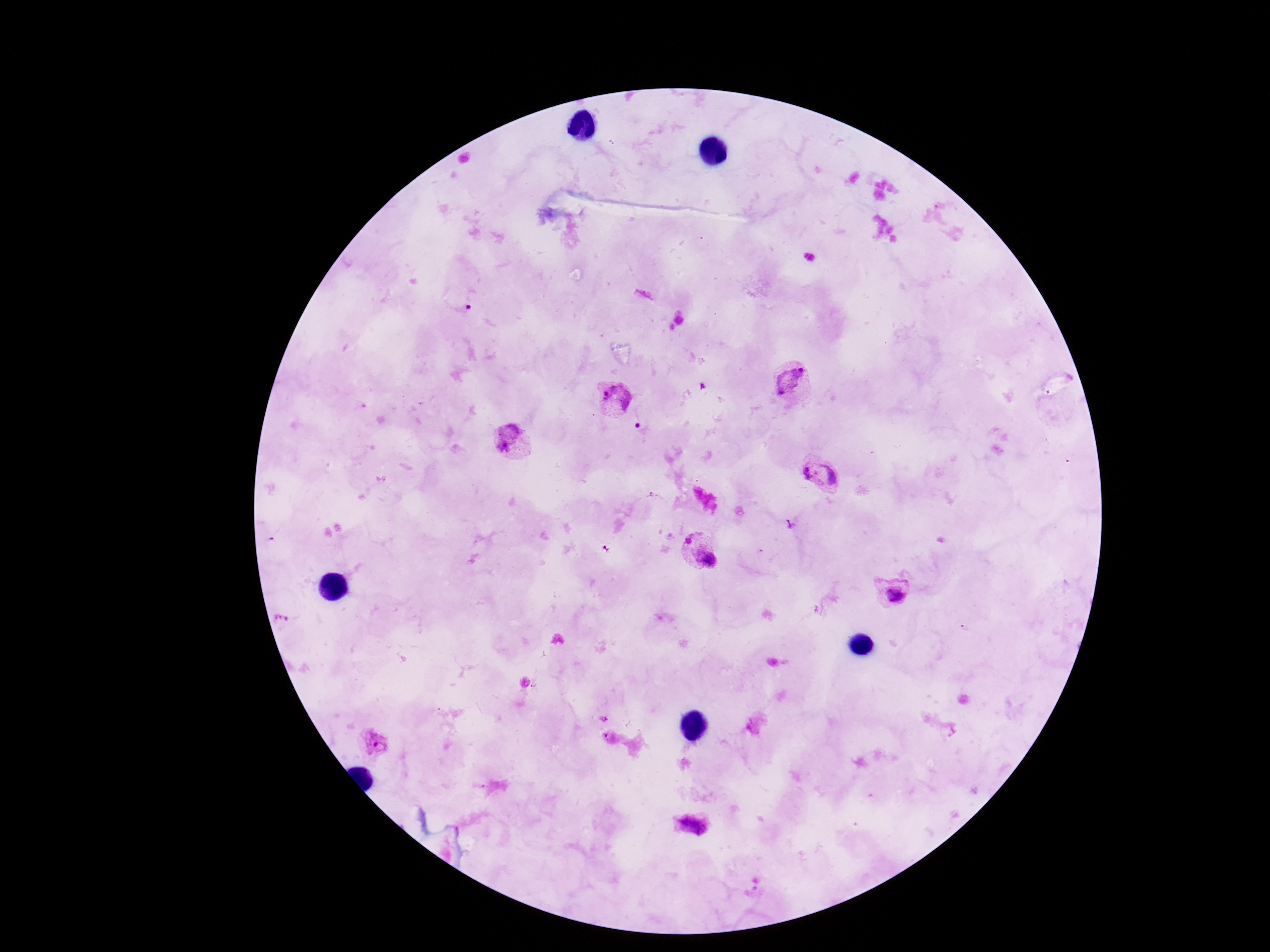
Approximate centers as (x, y) in pixels. Plasmodium parasite locations: (792, 383), (615, 398), (512, 441), (820, 475), (701, 552), (892, 592), (373, 742), (690, 825). Smartphone photograph taken through the microscope eyepiece. 100x magnification. Giemsa-stained preparation. Thick peripheral-blood smear. Single field of view. Image is 1270×952 pixels. Patient malaria status: infected.